Classify this cell by malaria status.
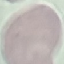

It is uninfected.

Summary:
  - Stain: Giemsa
  - Preparation: thin blood film
  - Image type: cell patch, automatically extracted from a larger field of view and resized to 64 × 64 pixels
  - Capture: smartphone camera at the microscope eyepiece